State the preparation type.
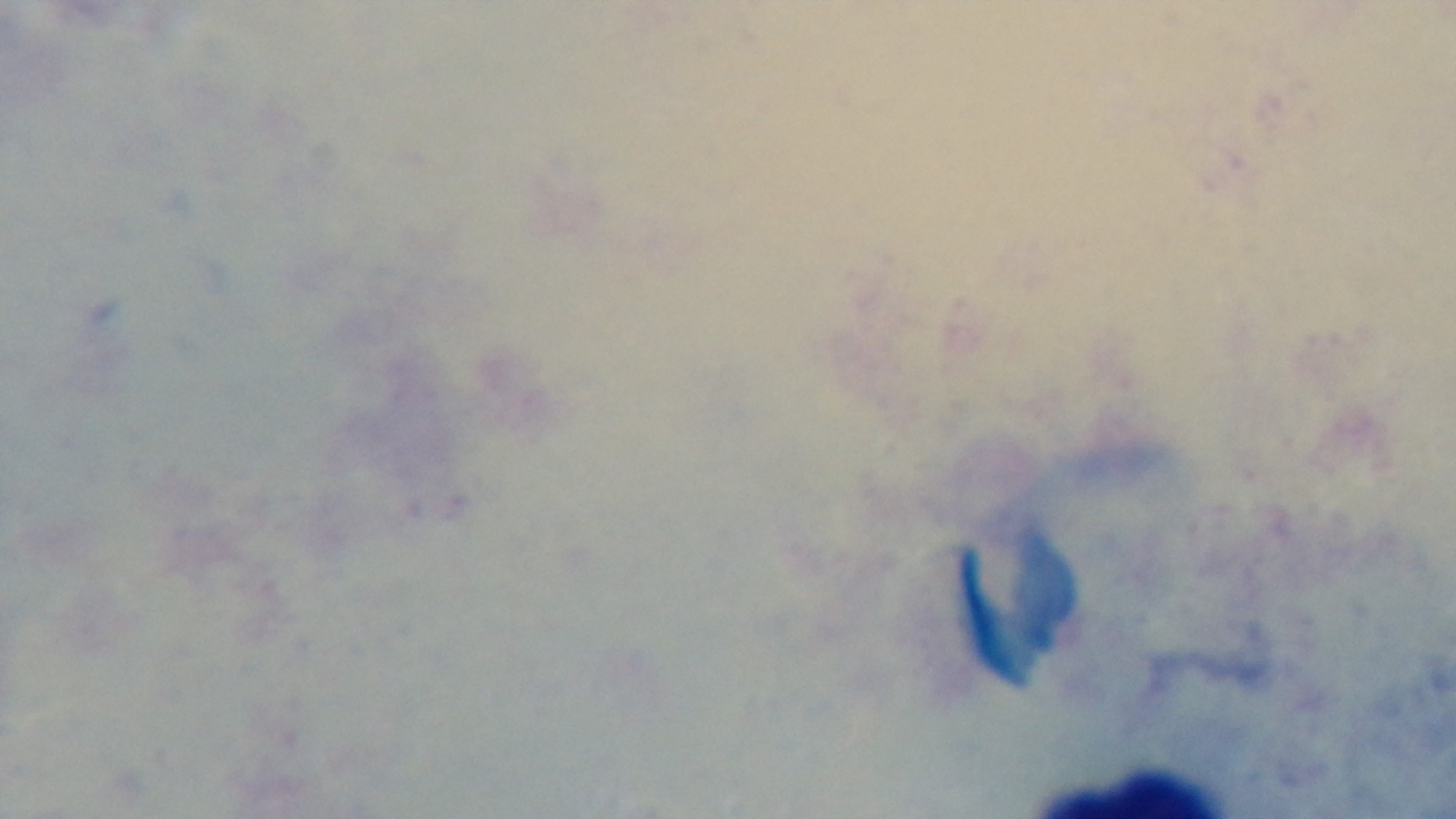

A thick smear.

100x oil-immersion objective. Malaria status: uninfected. Light microscopy. Captured with a mounted 4K digital camera. Giemsa-stained. One field from the slide.